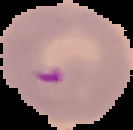
Summary:
  - Preparation: thin blood smear
  - Malaria status: parasitized
  - Image type: segmented cell region with the area outside set to black
  - Image size: 133×130 pixels